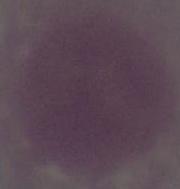

Captured at 1000x magnification. Micrograph. A red blood cell is shown.